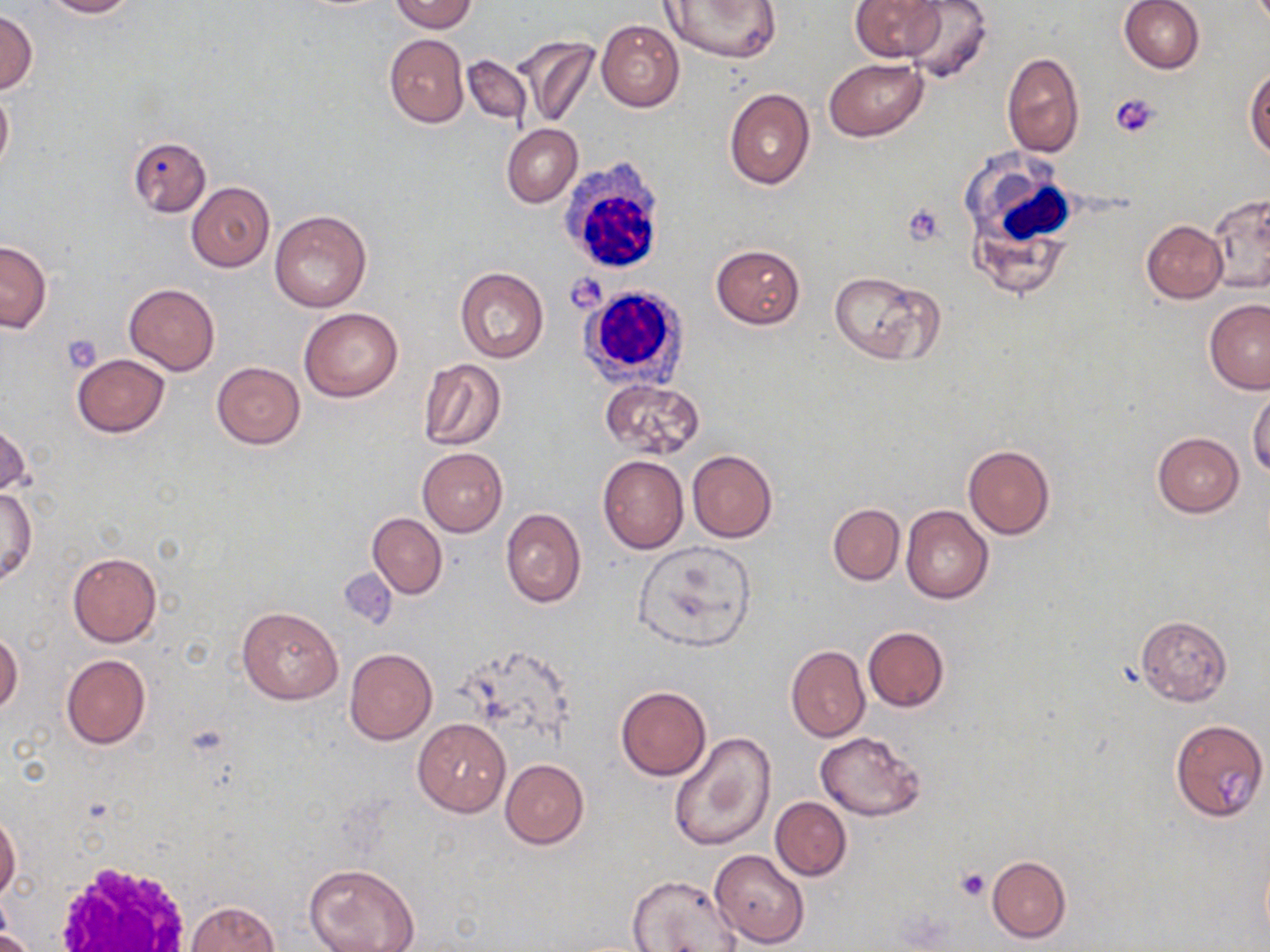

Approximate bounding boxes as [x1, y1, x2, y2] in pixels. White blood cell locations: [960, 148, 1079, 291], [557, 156, 670, 277], [578, 284, 692, 388], [51, 857, 196, 951]. Platelet locations: [1112, 94, 1161, 138], [901, 203, 947, 247], [565, 273, 607, 312], [62, 334, 103, 373], [956, 867, 989, 901]. Uninfected red blood cell locations: [38, 0, 137, 17], [387, 0, 477, 32], [661, 0, 780, 63], [850, 0, 944, 60], [899, 0, 993, 83], [1120, 0, 1205, 74], [0, 8, 37, 95], [595, 19, 683, 113], [384, 34, 469, 127], [513, 35, 598, 130], [1001, 51, 1085, 158], [462, 54, 531, 124], [824, 57, 928, 141], [1245, 67, 1270, 159], [0, 85, 13, 177], [724, 88, 815, 189], [502, 124, 582, 208], [128, 136, 211, 217], [187, 182, 275, 271], [1207, 190, 1269, 294], [270, 209, 372, 313], [1142, 219, 1227, 302], [0, 240, 51, 332], [710, 245, 805, 328], [454, 267, 548, 363], [827, 270, 943, 365], [124, 283, 219, 375], [1204, 299, 1269, 393], [299, 307, 403, 402], [71, 354, 170, 437], [417, 359, 507, 451], [211, 362, 304, 449], [599, 379, 705, 460], [1248, 386, 1270, 479], [1, 417, 29, 498], [1153, 431, 1245, 515], [962, 443, 1055, 540], [418, 448, 507, 535], [687, 450, 778, 543], [598, 455, 688, 554], [603, 477, 702, 606], [1, 486, 36, 586], [828, 504, 904, 584], [901, 504, 993, 604], [500, 508, 586, 607], [367, 512, 447, 598], [631, 540, 757, 653], [68, 552, 162, 647], [237, 605, 343, 704], [1135, 615, 1232, 706], [862, 626, 950, 710], [0, 630, 22, 717], [786, 646, 870, 742], [344, 648, 437, 745], [61, 654, 151, 750], [616, 686, 711, 780], [1170, 718, 1267, 822], [412, 719, 511, 817], [815, 731, 925, 820], [669, 732, 775, 853], [500, 758, 588, 848], [770, 797, 851, 881], [0, 813, 21, 900], [709, 849, 809, 948], [986, 856, 1071, 943], [305, 864, 419, 952], [627, 874, 742, 952], [185, 901, 279, 952], [0, 929, 33, 952]. Slide-level diagnosis: negative for blood parasites. Light microscopy. May-Grünwald-Giemsa stain. Single field of view. Thin blood smear. Image is 1270×952 pixels. Captured at 1000x magnification.